Outline each blood parasite and name the species.
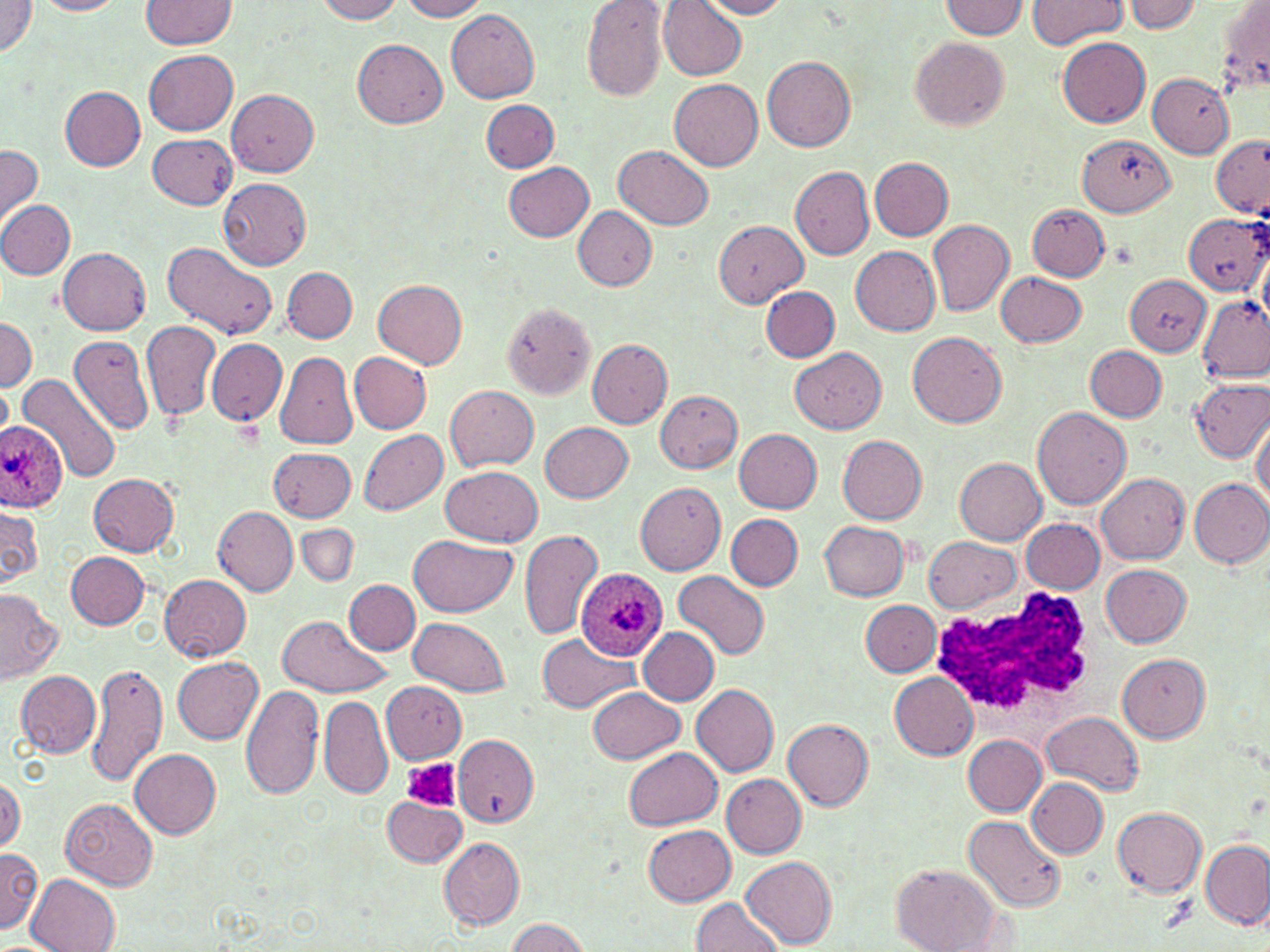

Approximate bounding boxes as (x1,y1)-(x2,y2) corner pairs in pixels.
Plasmodium ovale-infected red blood cells: (0,419)-(67,512), (579,567)-(667,671).
No Plasmodium falciparum, Plasmodium malariae, Plasmodium vivax, Babesia divergens, or Trypanosoma brucei observed.

Summary:
  - Uninfected red blood cell locations: (0,0)-(37,56), (37,0)-(127,16), (141,0)-(237,49), (315,0)-(405,23), (399,0)-(489,21), (697,0)-(792,19), (1027,0)-(1128,46), (1121,0)-(1204,34), (1215,0)-(1269,100), (939,1)-(1028,37), (582,2)-(669,103), (658,2)-(746,80), (446,9)-(542,103), (910,36)-(1011,131), (1058,37)-(1151,129), (353,40)-(448,128), (143,49)-(238,134), (761,55)-(857,151), (1147,73)-(1234,158), (669,79)-(764,170), (60,86)-(146,170), (228,88)-(319,177), (481,99)-(560,172), (148,133)-(238,209), (1078,135)-(1175,216), (1211,138)-(1270,217), (0,144)-(42,227), (614,146)-(714,230), (870,157)-(953,240), (504,162)-(594,242), (790,166)-(874,260), (220,178)-(311,269), (0,201)-(75,279), (1027,202)-(1110,281), (572,206)-(658,291), (1182,213)-(1268,295), (927,218)-(1015,315), (714,220)-(808,307), (163,242)-(279,340), (851,246)-(941,336), (57,248)-(151,335), (283,268)-(358,343), (996,271)-(1087,347), (1124,277)-(1210,352), (374,280)-(467,368), (761,285)-(840,362), (1198,295)-(1268,380), (502,304)-(596,400), (0,316)-(36,393), (141,320)-(220,421), (908,330)-(1007,426), (68,334)-(154,436), (207,338)-(287,426), (587,339)-(673,429), (789,345)-(886,433), (1085,345)-(1166,421), (274,350)-(358,450), (349,352)-(432,433), (17,375)-(121,488), (1188,379)-(1270,464), (0,381)-(13,444), (446,385)-(538,471), (656,389)-(744,473), (1031,406)-(1132,509), (1252,415)-(1270,507), (540,421)-(633,503), (359,429)-(448,515), (734,429)-(823,513), (838,435)-(928,524), (268,448)-(356,521), (955,457)-(1048,545), (441,465)-(542,546), (88,473)-(180,555), (1096,473)-(1190,563), (1187,477)-(1269,568), (635,482)-(726,575), (0,505)-(41,591), (214,506)-(299,595), (726,515)-(803,591), (1021,519)-(1104,594), (819,521)-(910,601), (298,524)-(358,584), (518,528)-(605,641), (410,535)-(517,618), (924,537)-(1020,613), (66,552)-(150,629), (1101,564)-(1192,646), (675,571)-(770,658), (160,574)-(251,660), (345,579)-(419,655), (0,590)-(63,685), (859,599)-(940,676), (275,613)-(390,696), (410,617)-(512,697), (638,627)-(718,705), (539,634)-(641,713), (1117,655)-(1210,742), (172,656)-(263,743), (84,659)-(168,787), (16,671)-(100,756), (890,672)-(978,759), (381,681)-(466,762), (241,682)-(325,801), (691,684)-(779,775), (587,687)-(686,764), (319,696)-(392,799), (1043,711)-(1142,797), (784,717)-(874,811), (963,735)-(1046,815), (454,736)-(538,826), (625,746)-(722,830), (130,749)-(221,838), (722,773)-(807,859), (0,775)-(22,852), (1027,778)-(1107,858), (381,796)-(466,867), (61,797)-(157,889), (1112,806)-(1208,897), (964,815)-(1065,913), (644,825)-(736,906), (438,837)-(526,929), (1200,840)-(1268,928), (1,848)-(43,935), (741,854)-(836,948), (891,863)-(1004,952), (25,873)-(121,951), (691,897)-(784,951), (505,918)-(592,952)
  - Platelet locations: (404,758)-(460,811)
  - White blood cell locations: (927,582)-(1100,734)
  - Slide-level diagnosis: Plasmodium ovale
  - Magnification: 1000x
  - Field of view: single
  - Modality: optical microscopy
  - Image size: 1270×952 pixels
  - Preparation: thin blood film
  - Stain: May-Grünwald-Giemsa